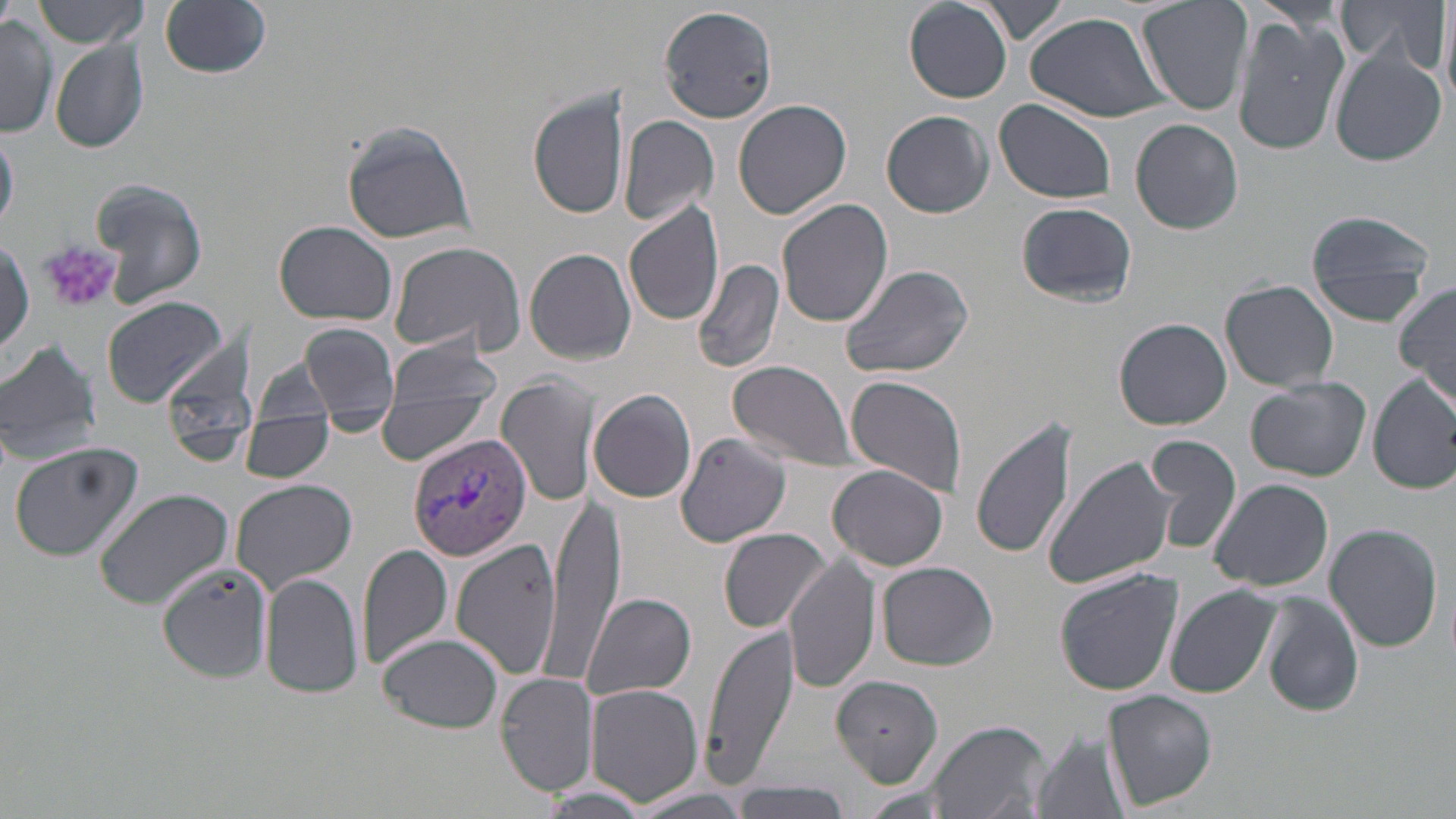
Approximate bounding boxes as (x1,y1)-(x2,y2) corner pairs in pixels. Platelet locations: (40,241)-(122,314). Uninfected red blood cell locations: (31,0)-(151,47), (904,0)-(1013,103), (975,0)-(1069,44), (1137,0)-(1253,116), (1338,0)-(1449,76), (160,1)-(271,79), (1438,2)-(1456,112), (658,3)-(778,125), (1024,8)-(1174,125), (1232,12)-(1350,158), (1,15)-(57,140), (50,38)-(149,154), (1328,48)-(1447,166), (529,90)-(630,220), (733,99)-(853,220), (993,99)-(1118,205), (882,110)-(993,218), (618,115)-(719,226), (1130,118)-(1244,234), (339,120)-(476,244), (0,126)-(18,233), (89,178)-(209,309), (775,197)-(893,329), (623,199)-(725,328), (1016,201)-(1137,307), (1304,207)-(1437,325), (273,220)-(398,326), (1,237)-(33,361), (387,240)-(524,358), (524,247)-(638,366), (692,257)-(786,375), (839,262)-(975,381), (1218,280)-(1339,392), (1394,283)-(1456,403), (99,294)-(229,408), (1115,318)-(1233,430), (301,323)-(398,421), (381,336)-(502,414), (0,338)-(103,466), (253,359)-(337,421), (728,359)-(858,469), (1368,372)-(1456,493), (497,374)-(595,508), (846,374)-(967,499), (1245,378)-(1371,481), (590,388)-(698,504), (374,400)-(488,462), (239,415)-(335,482), (313,415)-(395,435), (969,415)-(1079,559), (673,434)-(792,548), (1147,434)-(1239,555), (8,442)-(142,561), (1043,454)-(1178,590), (828,464)-(949,571), (1209,477)-(1334,592), (230,478)-(358,592), (549,484)-(622,674), (93,487)-(235,610), (1322,523)-(1444,653), (719,527)-(831,633), (443,539)-(564,682), (357,542)-(455,670), (785,556)-(879,693), (877,561)-(997,671), (156,563)-(272,683), (1054,568)-(1184,696), (261,573)-(364,700), (1165,587)-(1280,698), (583,592)-(696,701), (1259,594)-(1365,717), (699,625)-(799,793), (377,634)-(503,734), (496,672)-(600,794), (831,673)-(944,786), (584,684)-(704,806), (1103,690)-(1217,810), (925,719)-(1050,819), (1032,730)-(1130,819), (733,780)-(852,819), (537,785)-(656,815), (623,787)-(757,818). Plasmodium vivax-infected red blood cell locations: (407,432)-(532,561). Slide-level diagnosis: Plasmodium vivax. One field of a larger specimen. Captured at 1000x magnification. May-Grünwald-Giemsa-stained preparation. Image is 1456×819 pixels. Thin blood smear. Optical microscopy.